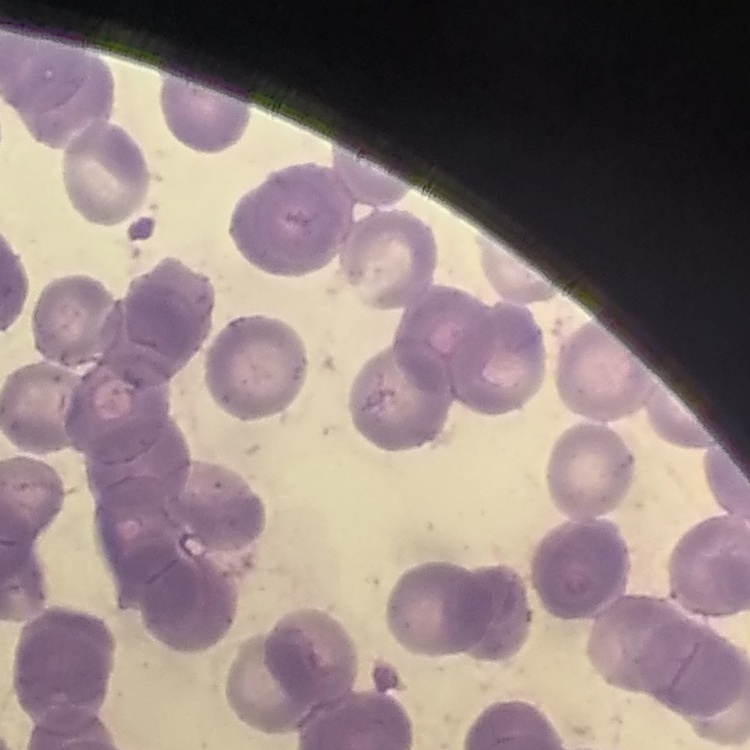

Summary:
  - Red blood cell morphology: rouleaux formation
  - Image type: square crop of a larger photomicrograph
  - Preparation: thin blood film
  - Stain: Field's or Giemsa